Report the malaria status of this cell.
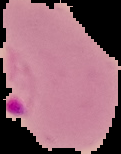
Parasitized.

Image is 121×154 pixels. From a thin blood smear. The area outside the segmented cell region is set to black.